Classify this cell by malaria status.
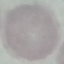
It is uninfected.

Summary:
  - Preparation: thin blood smear
  - Capture: smartphone camera at the microscope eyepiece
  - Stain: Giemsa
  - Image type: cell patch, automatically extracted from a larger field of view and resized to 64 × 64 pixels